Identify the cell.
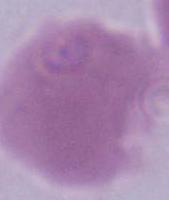

An erythrocyte.

Captured at 1000x magnification. Micrograph.